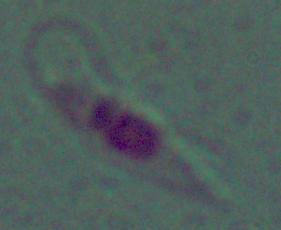
identification = Leishmania
magnification = 1000x
modality = photomicrograph